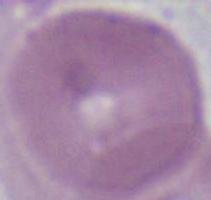
{
  "identification": "erythrocyte",
  "modality": "photomicrograph",
  "magnification": "1000x"
}